Locate every Plasmodium parasite.
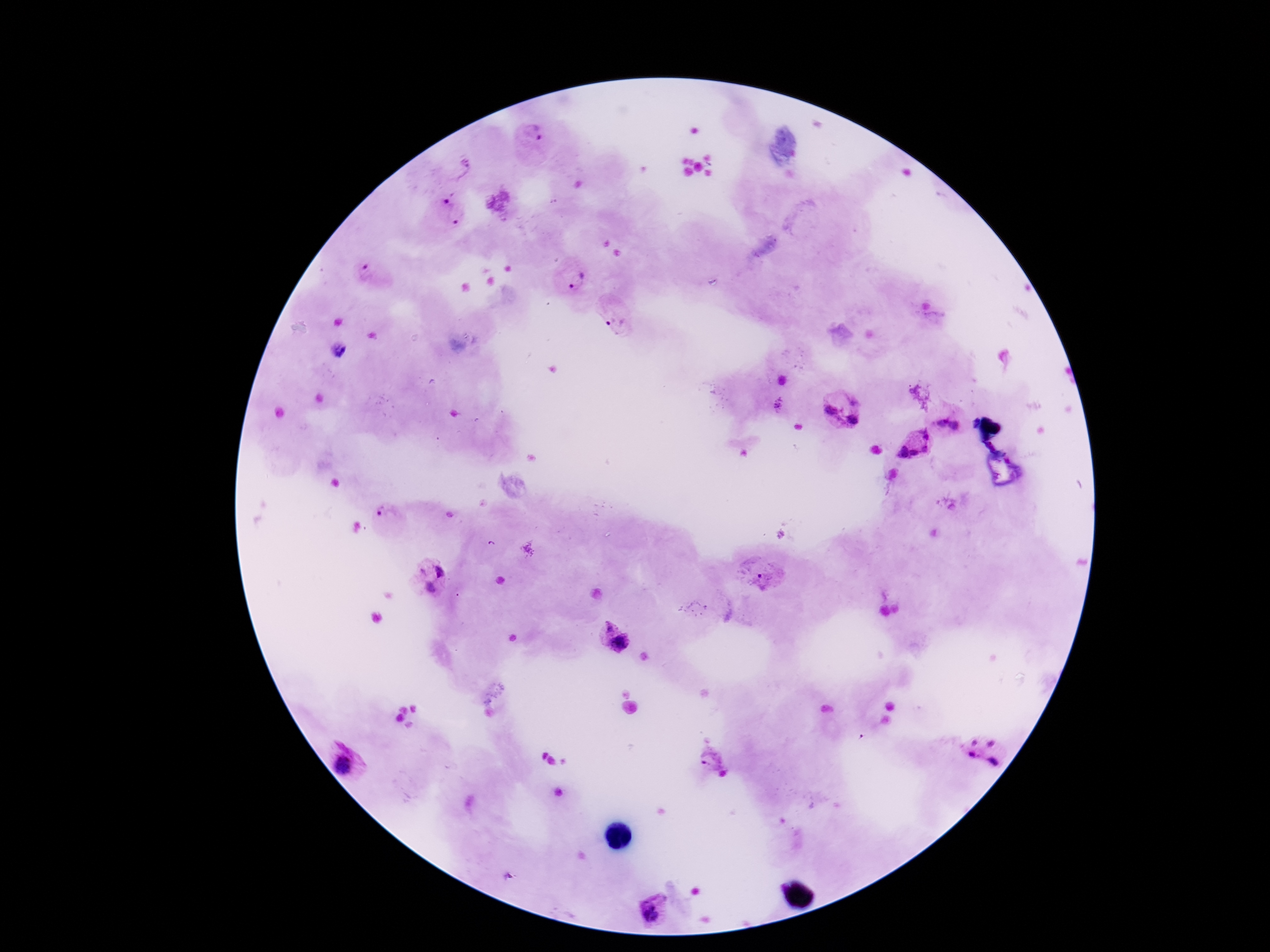

Approximate centers as {x, y} in pixels.
Plasmodium parasites: {534, 132}, {465, 169}, {446, 197}, {457, 220}, {365, 274}, {577, 283}, {619, 321}, {338, 349}, {779, 404}, {831, 411}, {852, 420}, {942, 422}, {957, 427}, {924, 434}, {925, 449}, {903, 452}, {913, 452}, {388, 514}, {421, 570}, {441, 570}, {761, 578}, {428, 588}, {607, 629}, {620, 643}, {973, 740}, {991, 741}, {972, 754}, {709, 759}, {994, 763}, {345, 765}, {722, 773}, {651, 911}.

Summary:
  - Field of view: one from this slide
  - Image size: 1270×952 pixels
  - Magnification: 100x
  - Preparation: thick blood film
  - Capture: smartphone camera through the microscope eyepiece
  - Patient malaria status: positive
  - Stain: Giemsa